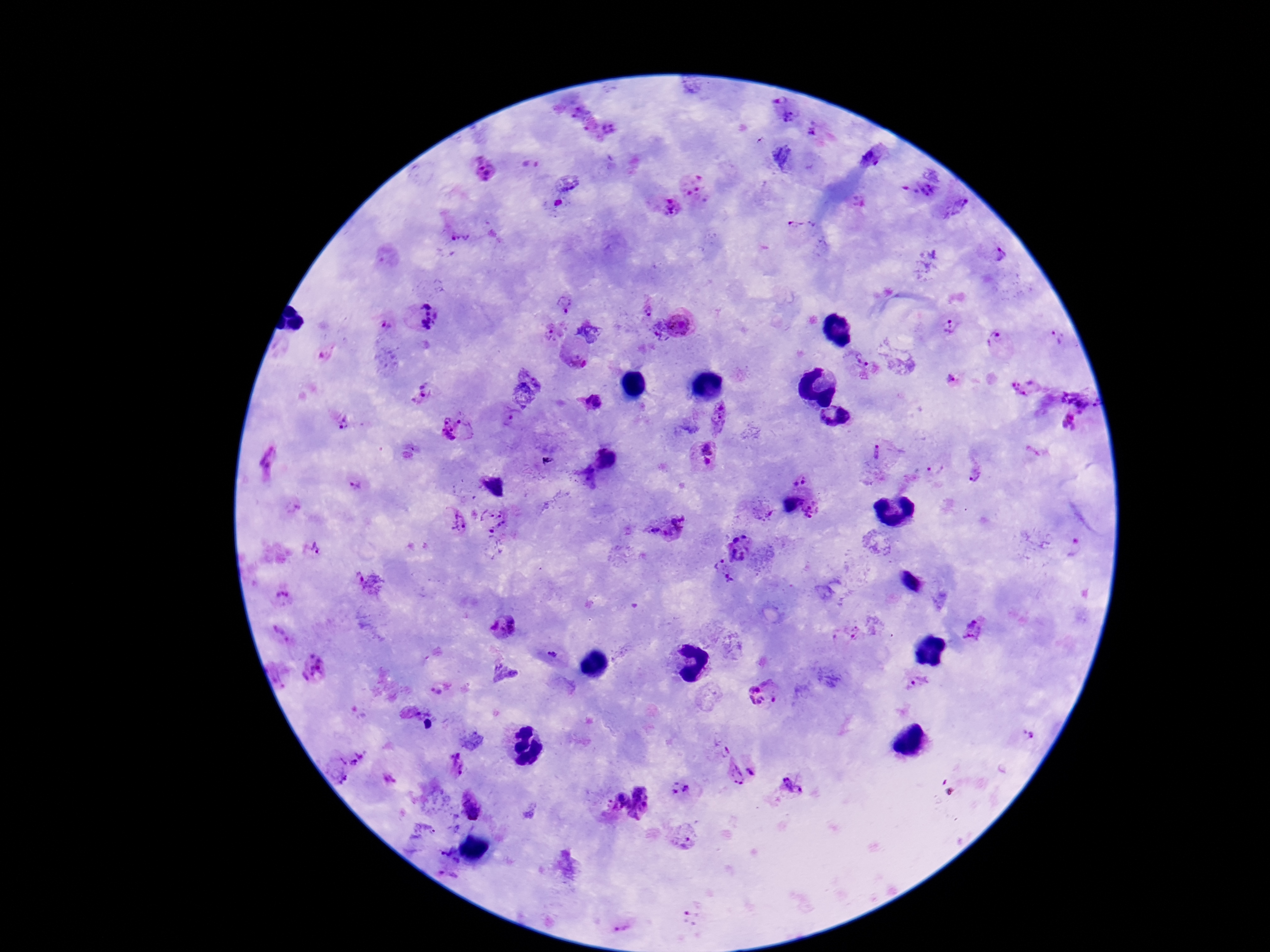

{
  "field_of_view": "one from this slide",
  "capture": "smartphone camera through the microscope eyepiece",
  "image_size": "1270×952 pixels",
  "stain": "Giemsa",
  "patient_malaria_status": "infected",
  "magnification": "100x",
  "plasmodium_parasite_locations": "approximate centers as (x, y) in pixels: (775, 98), (574, 114), (789, 117), (606, 130), (815, 133), (873, 157), (782, 158), (530, 165), (482, 167), (699, 189), (919, 192), (669, 207), (958, 208), (797, 227), (461, 239), (998, 255), (563, 302), (646, 306), (418, 316), (681, 323), (948, 324), (381, 327), (553, 331), (660, 331), (593, 332), (1058, 337), (997, 339), (574, 357), (863, 359), (955, 380), (1022, 390), (422, 394), (1080, 395), (589, 401), (835, 416), (720, 417), (346, 422), (1070, 422), (456, 429), (877, 451), (707, 456), (606, 458), (549, 462), (935, 469), (975, 473), (583, 478), (799, 479), (355, 484), (812, 508), (761, 511), (454, 521), (497, 525), (668, 525), (315, 546), (740, 548), (1074, 549), (723, 571), (369, 584), (282, 595), (504, 626), (279, 632), (846, 633), (972, 633), (556, 656), (314, 667), (502, 674), (276, 676), (918, 683), (440, 690), (765, 693), (1030, 735), (362, 759), (459, 765), (338, 770), (734, 773), (750, 773), (391, 777), (791, 787), (682, 790), (617, 798), (469, 804), (642, 804), (682, 837), (447, 862), (693, 914), (622, 922)",
  "preparation": "thick blood film"
}